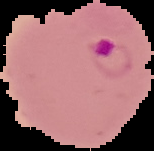

result = malaria parasites identified
image type = segmented cell region on a black background
preparation = thin blood smear
image size = 154×151 pixels